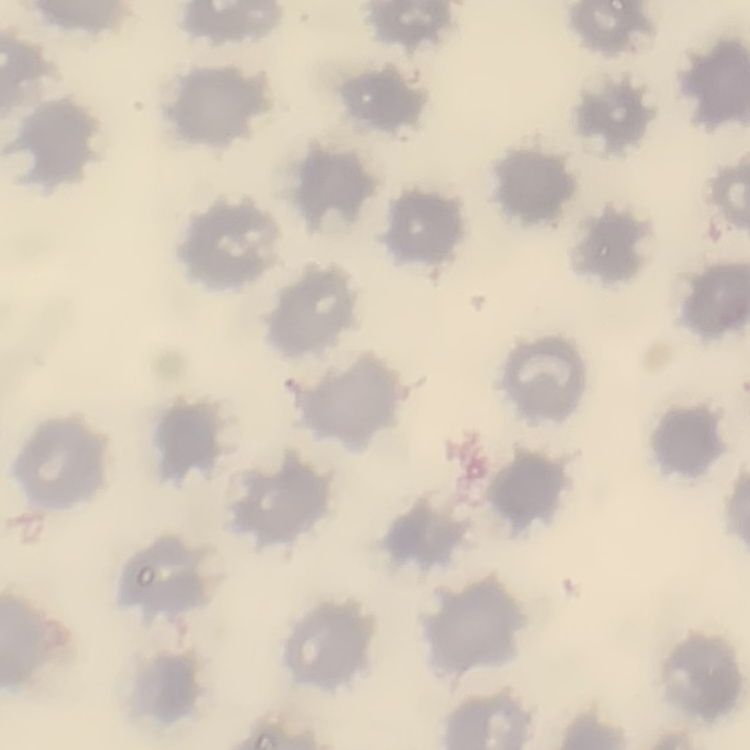

The red blood cells exhibit no rouleaux formation. Field's or Giemsa stain. Thin blood smear. One tile cut from a larger photomicrograph.